Report the malaria status of this cell.
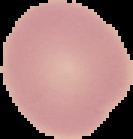

It is uninfected.

Summary:
  - Image size: 133×139 pixels
  - Image type: segmented cell region with the area outside set to black
  - Preparation: thin blood film